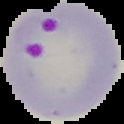
Summary:
  - Image size: 124×124 pixels
  - Image type: segmented cell region with the area outside set to black
  - Malaria status: parasitized
  - Preparation: thin blood film